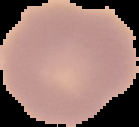
Summary:
  - Preparation: thin blood smear
  - Image size: 139×127 pixels
  - Image type: cell region segmented out of the field of view; surrounding area masked to black
  - Result: negative for Plasmodium parasites